Name the blood parasite species.
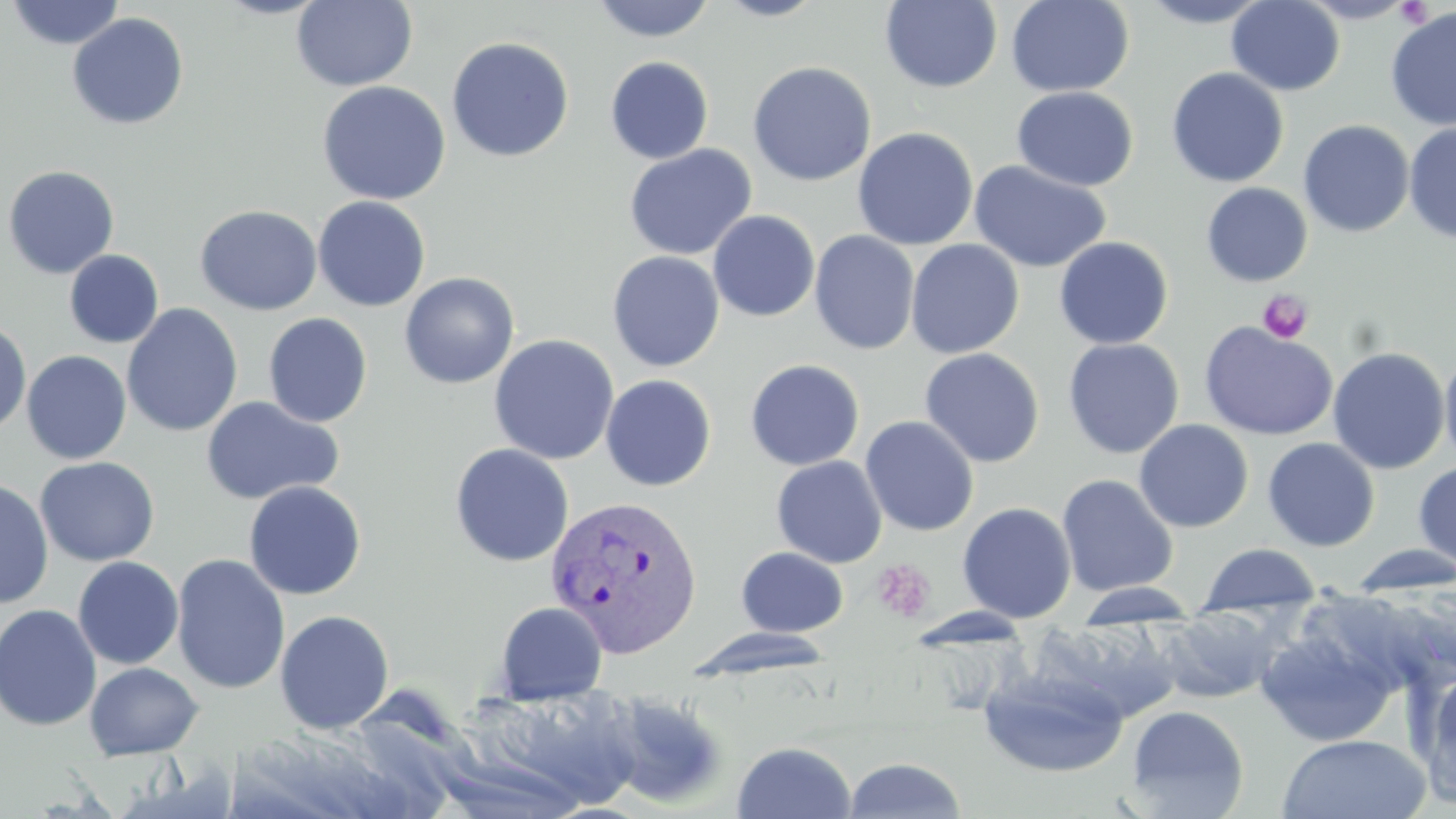

Plasmodium vivax.

Approximate bounding boxes as (x1, y1, x2, y2) in pixels. Platelet locations: (1395, 1, 1435, 28), (1257, 289, 1314, 344), (871, 559, 935, 623). Plasmodium vivax-infected red blood cell locations: (545, 493, 704, 657). Uninfected red blood cell locations: (292, 0, 418, 91), (590, 0, 717, 42), (712, 0, 829, 21), (1005, 0, 1135, 97), (1134, 0, 1276, 27), (1296, 0, 1420, 23), (6, 1, 126, 50), (880, 1, 1002, 93), (1227, 1, 1345, 95), (1385, 6, 1456, 131), (66, 12, 189, 130), (446, 36, 575, 162), (604, 56, 714, 164), (747, 61, 877, 187), (1166, 67, 1289, 188), (317, 81, 451, 205), (1012, 86, 1137, 191), (1298, 120, 1415, 238), (1403, 121, 1456, 245), (852, 127, 978, 250), (623, 144, 758, 261), (968, 160, 1112, 273), (2, 165, 120, 279), (1201, 182, 1312, 287), (312, 196, 431, 311), (195, 204, 322, 316), (707, 210, 820, 322), (809, 230, 920, 355), (1054, 236, 1173, 349), (905, 239, 1025, 359), (64, 250, 164, 348), (607, 251, 725, 372), (399, 272, 519, 389), (121, 303, 243, 438), (263, 312, 372, 427), (0, 319, 32, 436), (1199, 321, 1339, 441), (488, 334, 619, 465), (1063, 337, 1184, 459), (1327, 346, 1451, 475), (919, 347, 1045, 468), (1439, 349, 1456, 470), (21, 350, 132, 464), (744, 358, 865, 470), (600, 374, 717, 492), (200, 396, 344, 506), (860, 416, 979, 537), (1134, 419, 1254, 533), (1262, 437, 1380, 552), (449, 443, 574, 567), (35, 456, 160, 567), (771, 456, 887, 568), (1413, 461, 1456, 571), (1057, 474, 1179, 597), (0, 478, 54, 609), (243, 480, 367, 601), (957, 502, 1076, 623), (1196, 543, 1324, 617), (1346, 545, 1456, 597), (736, 547, 849, 637), (171, 553, 290, 695), (73, 556, 184, 670), (1070, 583, 1205, 622), (494, 601, 608, 705), (0, 604, 103, 731), (1152, 607, 1286, 704), (275, 610, 394, 734), (1031, 621, 1181, 723), (1254, 625, 1400, 747), (686, 626, 836, 682), (84, 662, 204, 760), (976, 665, 1130, 779), (1416, 668, 1456, 807), (475, 683, 647, 811), (598, 688, 732, 810), (1125, 705, 1249, 818), (1275, 733, 1431, 819), (732, 740, 857, 819), (842, 757, 967, 818). Optical microscopy. Single field of view. Image is 1456×819 pixels. May-Grünwald-Giemsa stain. Thin blood smear. Captured at 1000x magnification.